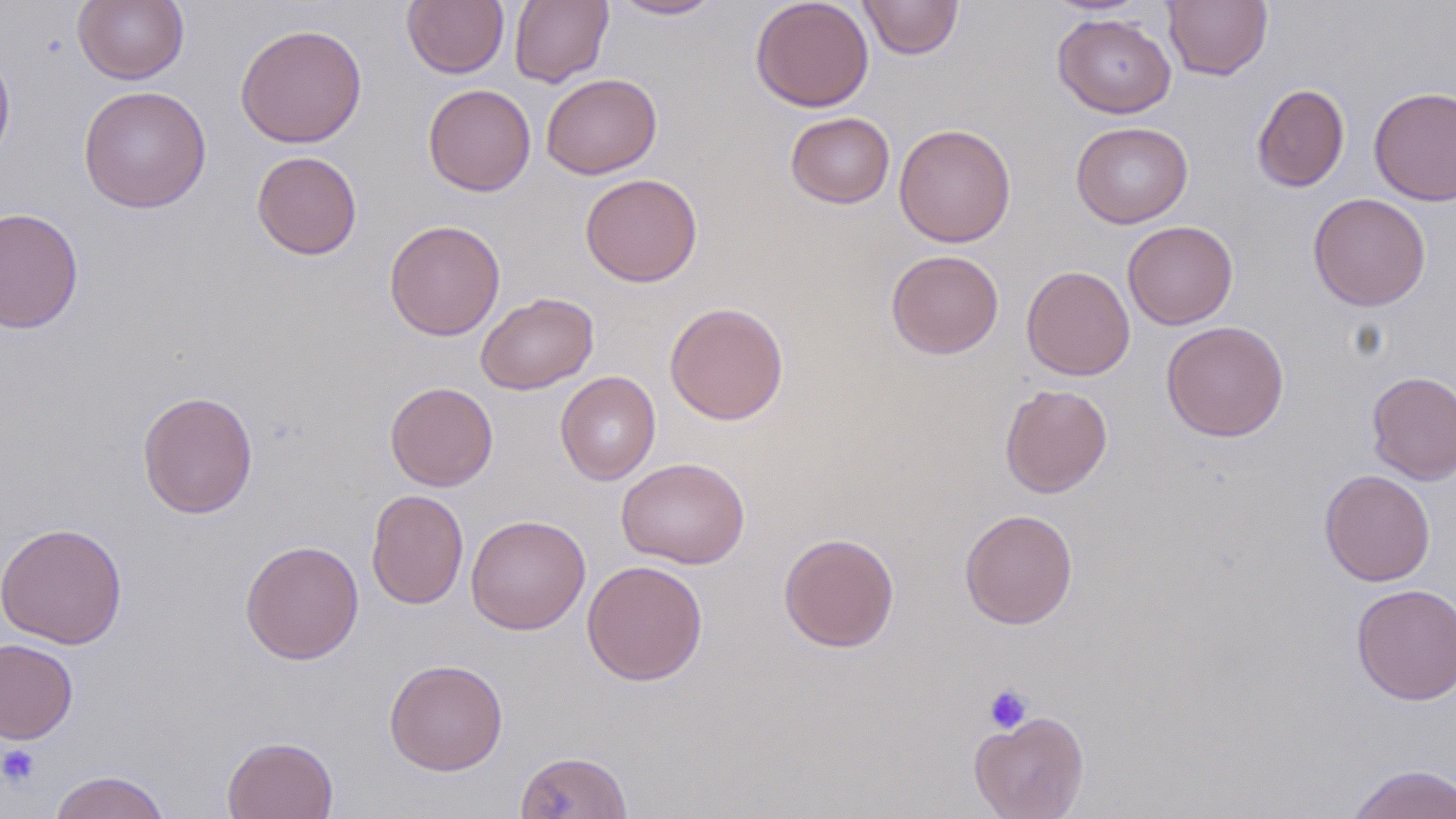 Approximate bounding boxes as named x1/y1/x2/y2 corners in pixels. Platelet locations: (x1=983, y1=683, x2=1034, y2=734), (x1=0, y1=743, x2=41, y2=788). Uninfected red blood cell locations: (x1=73, y1=0, x2=190, y2=85), (x1=402, y1=0, x2=509, y2=78), (x1=510, y1=0, x2=613, y2=88), (x1=608, y1=0, x2=722, y2=20), (x1=750, y1=0, x2=875, y2=113), (x1=858, y1=0, x2=964, y2=60), (x1=1163, y1=0, x2=1273, y2=81), (x1=1053, y1=13, x2=1176, y2=118), (x1=235, y1=23, x2=367, y2=148), (x1=0, y1=46, x2=15, y2=170), (x1=541, y1=73, x2=662, y2=179), (x1=423, y1=83, x2=536, y2=196), (x1=1252, y1=83, x2=1350, y2=192), (x1=78, y1=85, x2=211, y2=213), (x1=1368, y1=85, x2=1456, y2=206), (x1=785, y1=112, x2=895, y2=209), (x1=1071, y1=121, x2=1193, y2=228), (x1=894, y1=123, x2=1016, y2=248), (x1=251, y1=150, x2=362, y2=260), (x1=580, y1=173, x2=703, y2=287), (x1=1307, y1=192, x2=1431, y2=311), (x1=0, y1=206, x2=84, y2=334), (x1=384, y1=219, x2=505, y2=341), (x1=1122, y1=220, x2=1238, y2=329), (x1=886, y1=249, x2=1004, y2=359), (x1=1021, y1=265, x2=1135, y2=380), (x1=475, y1=291, x2=599, y2=394), (x1=664, y1=301, x2=789, y2=425), (x1=1161, y1=320, x2=1289, y2=442), (x1=1366, y1=370, x2=1456, y2=484), (x1=555, y1=371, x2=661, y2=485), (x1=385, y1=381, x2=498, y2=491), (x1=999, y1=383, x2=1113, y2=498), (x1=137, y1=390, x2=258, y2=519), (x1=616, y1=457, x2=750, y2=569), (x1=1319, y1=469, x2=1435, y2=587), (x1=366, y1=489, x2=469, y2=609), (x1=959, y1=508, x2=1078, y2=629), (x1=465, y1=514, x2=591, y2=634), (x1=0, y1=522, x2=128, y2=649), (x1=778, y1=532, x2=899, y2=652), (x1=240, y1=540, x2=364, y2=665), (x1=581, y1=559, x2=708, y2=686), (x1=1350, y1=584, x2=1456, y2=705), (x1=0, y1=638, x2=78, y2=744), (x1=384, y1=659, x2=508, y2=775), (x1=969, y1=710, x2=1090, y2=819), (x1=223, y1=736, x2=338, y2=819), (x1=514, y1=750, x2=632, y2=819), (x1=1345, y1=763, x2=1456, y2=819), (x1=48, y1=770, x2=171, y2=819). Slide-level diagnosis: negative for blood parasites. May-Grünwald-Giemsa-stained preparation. Thin blood film. One field of a larger specimen. Light microscopy. Image is 1456×819 pixels. 1000x magnification.